Comment on the morphology of the red blood cells.
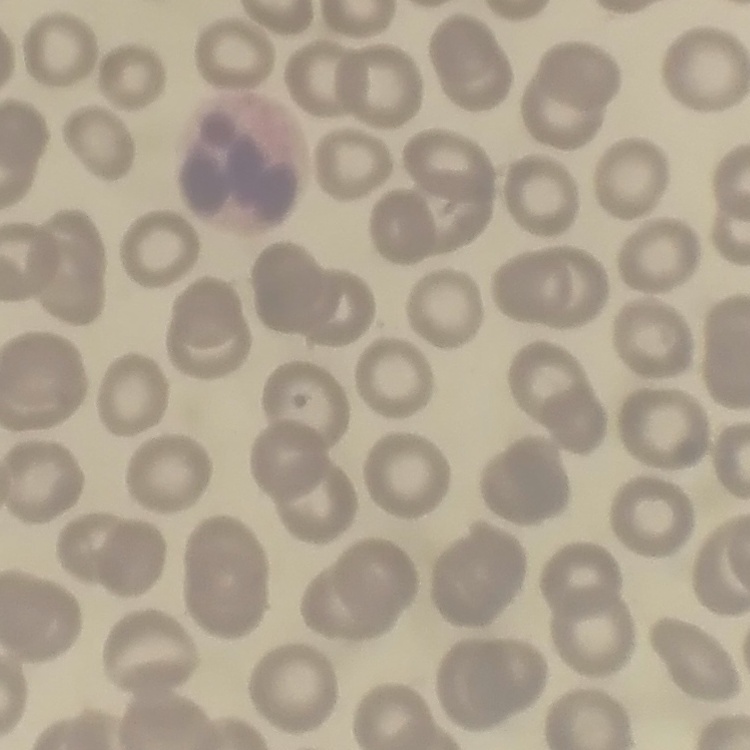
No rouleaux formation.

image type = one tile cut from a larger photomicrograph
stain = Field's or Giemsa
preparation = thin blood smear